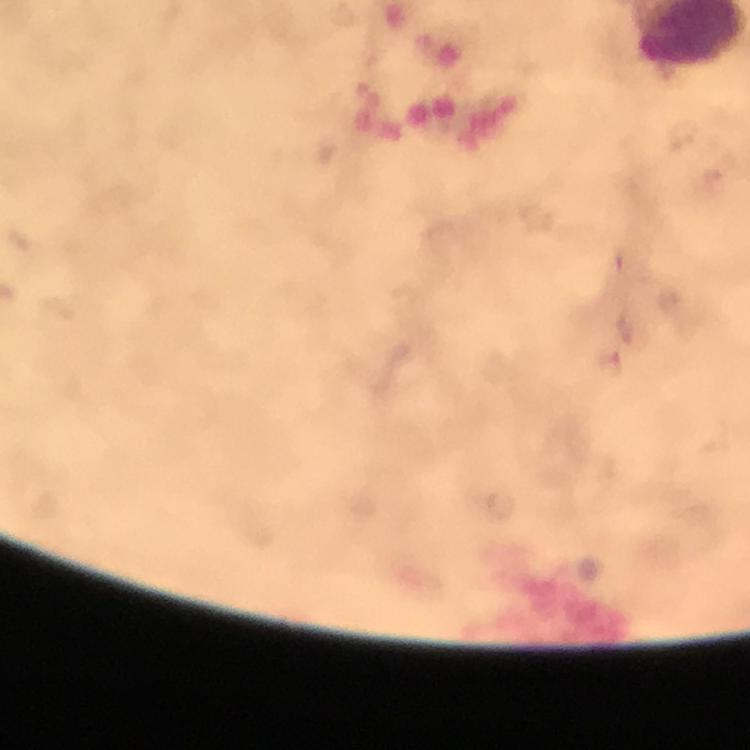

Approximate object centers, in pixels from the top-left corner.
Summary:
  - Malaria parasite locations: (x=612, y=364)
  - Context: from a malaria diagnostic workup
  - Preparation: thick smear
  - Stain: Giemsa
  - Cropped from: a single field of view
  - Image size: 750×750 pixels
  - Capture: smartphone mounted on the microscope
  - Magnification: 100x
  - Immersion oil: applied